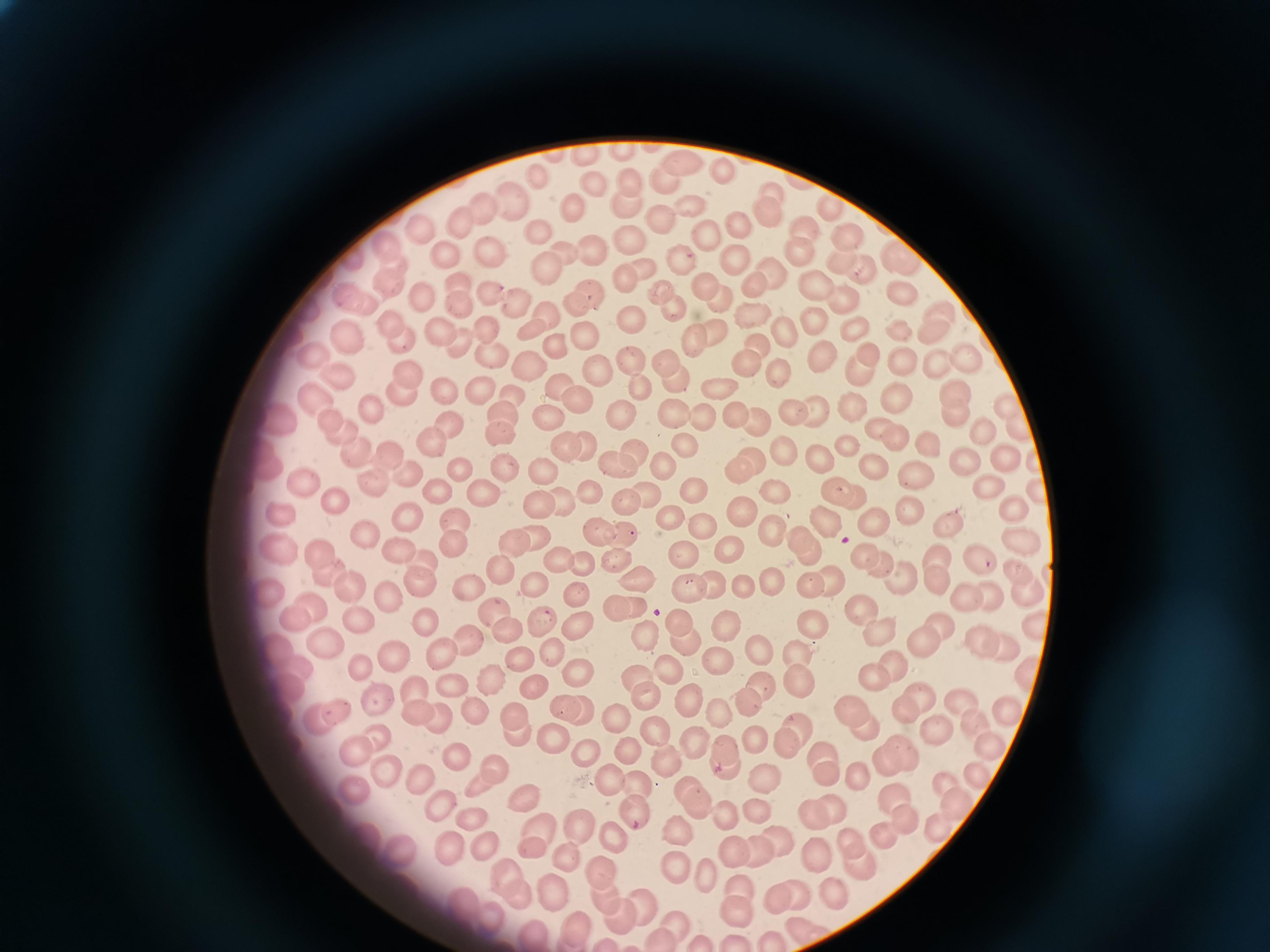
{
  "cell_locations": "approximate centers as [x, y] in pixels: [682, 161], [724, 171], [538, 179], [666, 180], [630, 184], [592, 187], [773, 192], [508, 199], [627, 204], [690, 205], [830, 206], [479, 208], [574, 212], [767, 213], [658, 219], [457, 222], [739, 226], [419, 228], [539, 229], [807, 230], [709, 233], [631, 238], [846, 238], [389, 247], [560, 250], [799, 250], [490, 251], [589, 251], [446, 252], [897, 255], [733, 257], [678, 258], [840, 259], [543, 269], [645, 269], [772, 269], [862, 271], [624, 273], [817, 281], [389, 283], [458, 283], [753, 283], [705, 286], [901, 289], [657, 290], [491, 294], [590, 294], [350, 295], [424, 295], [843, 298], [717, 300], [516, 302], [462, 303], [575, 305], [751, 308], [944, 309], [674, 310], [547, 316], [632, 316], [819, 319], [390, 320], [441, 326], [529, 327], [856, 327], [899, 329], [934, 331], [483, 332], [783, 332], [715, 333], [586, 335], [350, 337], [695, 337], [404, 341], [461, 345], [758, 345], [560, 348], [870, 349], [314, 354], [494, 356], [825, 357], [628, 358], [966, 358], [667, 359], [905, 359], [937, 361], [747, 363], [860, 367], [531, 369], [597, 370], [780, 372], [341, 374], [404, 378], [675, 379], [637, 384], [721, 385], [556, 386], [480, 388], [447, 389], [954, 391], [900, 392], [403, 393], [512, 394], [318, 398], [576, 399], [1008, 402], [371, 405], [855, 407], [675, 409], [820, 409], [621, 411], [791, 411], [737, 414], [956, 414], [453, 418], [703, 418], [549, 419], [500, 420], [758, 421], [283, 422], [1017, 425], [878, 426], [981, 426], [337, 430], [894, 436], [431, 440], [924, 441], [586, 442], [563, 446], [687, 446], [850, 446], [786, 450], [392, 452], [637, 453], [357, 454], [262, 456], [754, 457], [820, 457], [969, 459], [1005, 460], [614, 462], [665, 466], [504, 467], [741, 467], [878, 467], [462, 469], [545, 469], [920, 473], [405, 476], [370, 479], [989, 483], [308, 487], [837, 490], [696, 491], [772, 491], [441, 492], [589, 492], [1037, 492], [854, 495], [486, 496], [649, 497], [560, 500], [538, 502], [625, 503], [335, 504], [906, 505], [1015, 506], [282, 513], [405, 513], [746, 513], [873, 518], [454, 519], [948, 520], [670, 522], [829, 523], [707, 526], [593, 529], [772, 531], [623, 535], [368, 536], [539, 538], [810, 540], [1020, 541], [282, 542], [453, 543], [518, 544], [733, 551], [320, 552], [398, 554], [684, 555], [865, 555], [616, 556], [937, 556], [980, 558], [421, 559], [560, 561], [883, 562], [584, 566], [498, 567], [1017, 569], [327, 573], [901, 575], [833, 578], [422, 579], [938, 579], [641, 580], [535, 582], [812, 583], [349, 585], [773, 586], [464, 589], [717, 589], [748, 590], [1028, 590], [268, 592], [387, 593], [575, 593], [692, 593], [989, 594], [967, 596], [634, 604], [617, 608], [864, 609], [315, 611], [499, 612], [428, 617], [295, 618], [539, 619], [362, 621], [940, 622], [682, 623], [579, 624], [810, 625], [1033, 627], [876, 628], [724, 630], [506, 631], [643, 635], [922, 639], [981, 639], [685, 640], [468, 642], [1004, 644], [326, 647], [279, 648], [756, 651], [396, 652], [440, 652], [554, 653], [800, 653], [520, 658], [716, 661], [896, 664], [363, 667], [295, 668], [1025, 669], [674, 673], [634, 674], [580, 677], [872, 677], [493, 679], [450, 683], [799, 685], [531, 687], [287, 688], [413, 688], [760, 690], [644, 694], [917, 694], [378, 704], [691, 704], [744, 704], [957, 705], [903, 706], [562, 707], [335, 709], [1005, 709], [418, 711], [475, 711], [584, 711], [857, 711], [722, 712], [518, 717], [619, 717], [315, 720], [654, 722], [439, 723], [973, 725], [935, 727], [865, 729], [514, 731], [801, 733], [551, 734], [755, 738], [783, 743], [984, 744], [698, 745], [355, 747], [726, 747], [589, 749], [627, 749], [820, 755], [906, 755], [458, 758], [667, 758], [884, 762], [725, 765], [380, 768], [859, 771], [496, 772], [604, 772], [978, 772], [765, 776], [826, 776], [417, 779], [635, 782], [943, 786], [353, 787], [694, 796], [894, 798], [526, 801], [437, 804], [756, 805], [832, 806], [961, 806], [635, 808], [814, 811], [725, 813], [470, 818], [908, 819], [581, 826], [935, 827], [883, 831], [538, 833], [677, 835], [612, 840], [854, 840], [482, 842], [775, 842], [448, 846], [733, 850], [757, 850], [532, 851], [821, 856], [566, 858], [858, 863], [675, 868], [505, 875], [599, 875], [706, 877], [510, 890], [553, 891], [741, 891], [835, 894], [792, 895], [603, 897], [775, 898], [643, 907], [737, 913], [616, 916], [676, 921], [576, 926], [534, 931], [810, 931], [659, 941]",
  "stain": "Giemsa",
  "image_size": "1270×952 pixels",
  "capture": "smartphone through the microscope eyepiece",
  "preparation": "thin blood film",
  "field_of_view": "single"
}